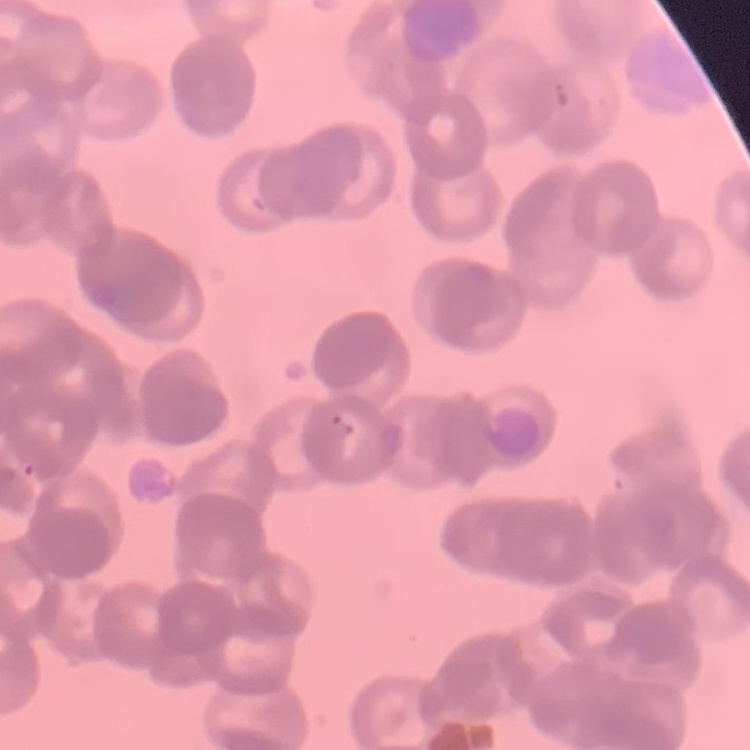
erythrocyte morphology = rouleaux formation
image type = square crop of a larger photomicrograph
stain = Field's or Giemsa
preparation = thin blood smear